State which parasite is depicted.
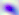
Toxoplasma gondii.

Captured at 400x magnification. Photomicrograph.